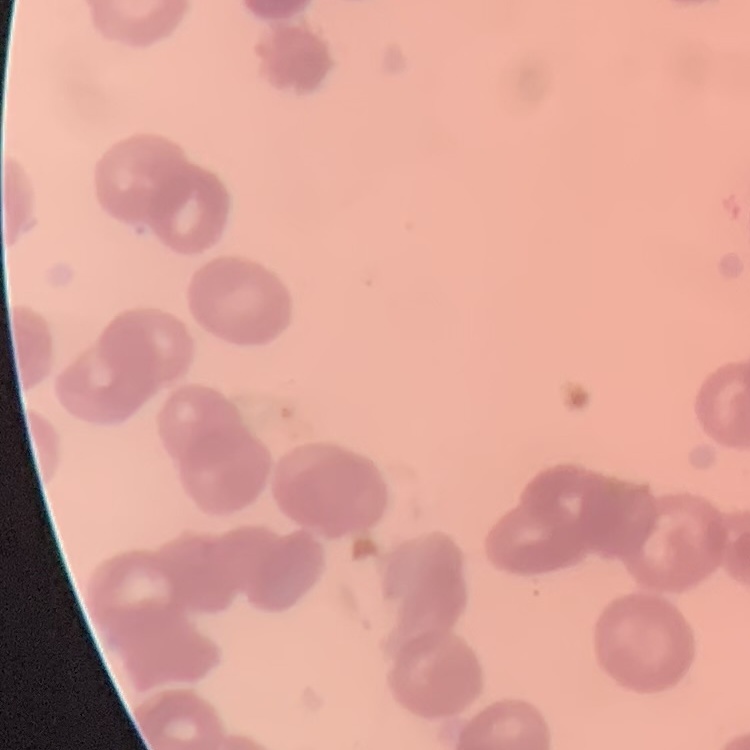 The red blood cells exhibit rouleaux formation. Square crop of a larger photomicrograph. Thin peripheral smear. Field's or Giemsa stain.